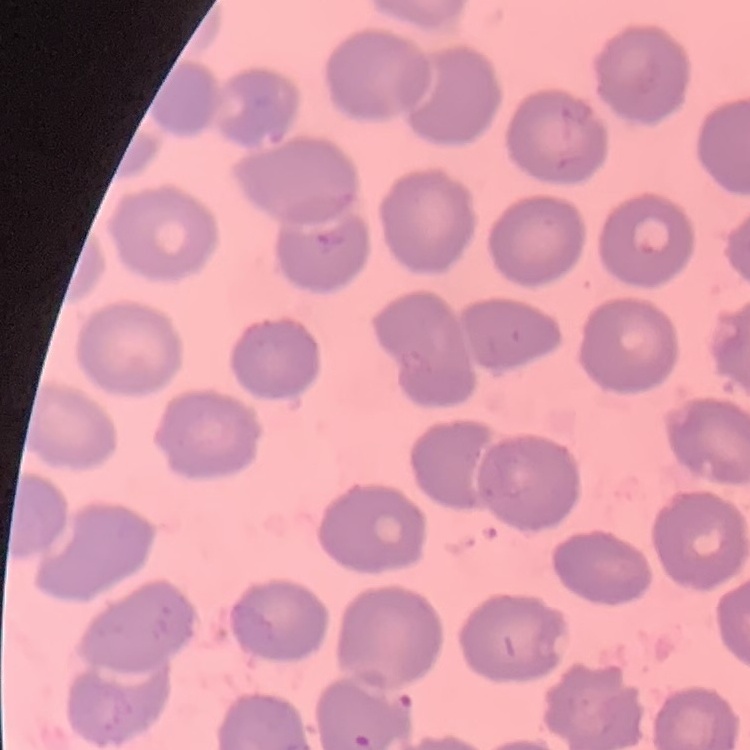
red blood cell morphology = no rouleaux formation
image type = square crop of a larger photomicrograph
stain = Field's or Giemsa
preparation = thin blood film